Locate every Plasmodium parasite.
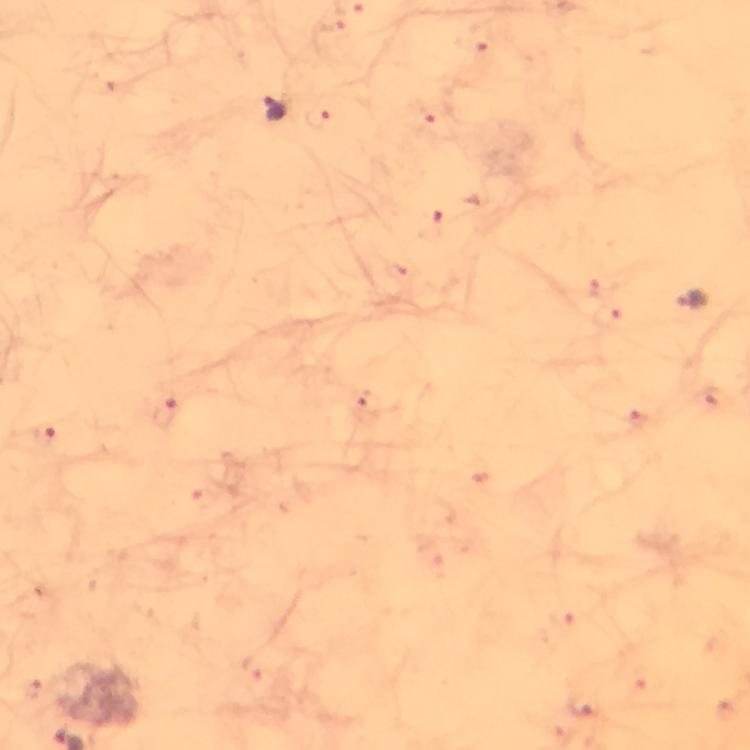
Approximate centers as {x, y} in pixels.
Plasmodium parasites: {276, 108}, {693, 299}.

Summary:
  - Stain: Giemsa
  - Context: from a diagnostic examination for malaria
  - Capture: smartphone mounted on the microscope
  - Preparation: thick blood film
  - Immersion oil: applied
  - Magnification: 100x
  - Image size: 750×750 pixels
  - Cropped from: one field of view